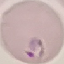
Summary:
  - Malaria status: parasitized
  - Image type: automatically extracted cell patch, resized to 64 × 64 pixels
  - Preparation: thin blood smear
  - Capture: smartphone camera at the microscope eyepiece
  - Stain: Giemsa